Report the malaria status of this cell.
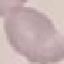

It is uninfected.

Automatically extracted cell patch, resized to 64 × 64 pixels. Photographed with a smartphone camera at the microscope eyepiece. Giemsa-stained preparation. Thin blood smear.